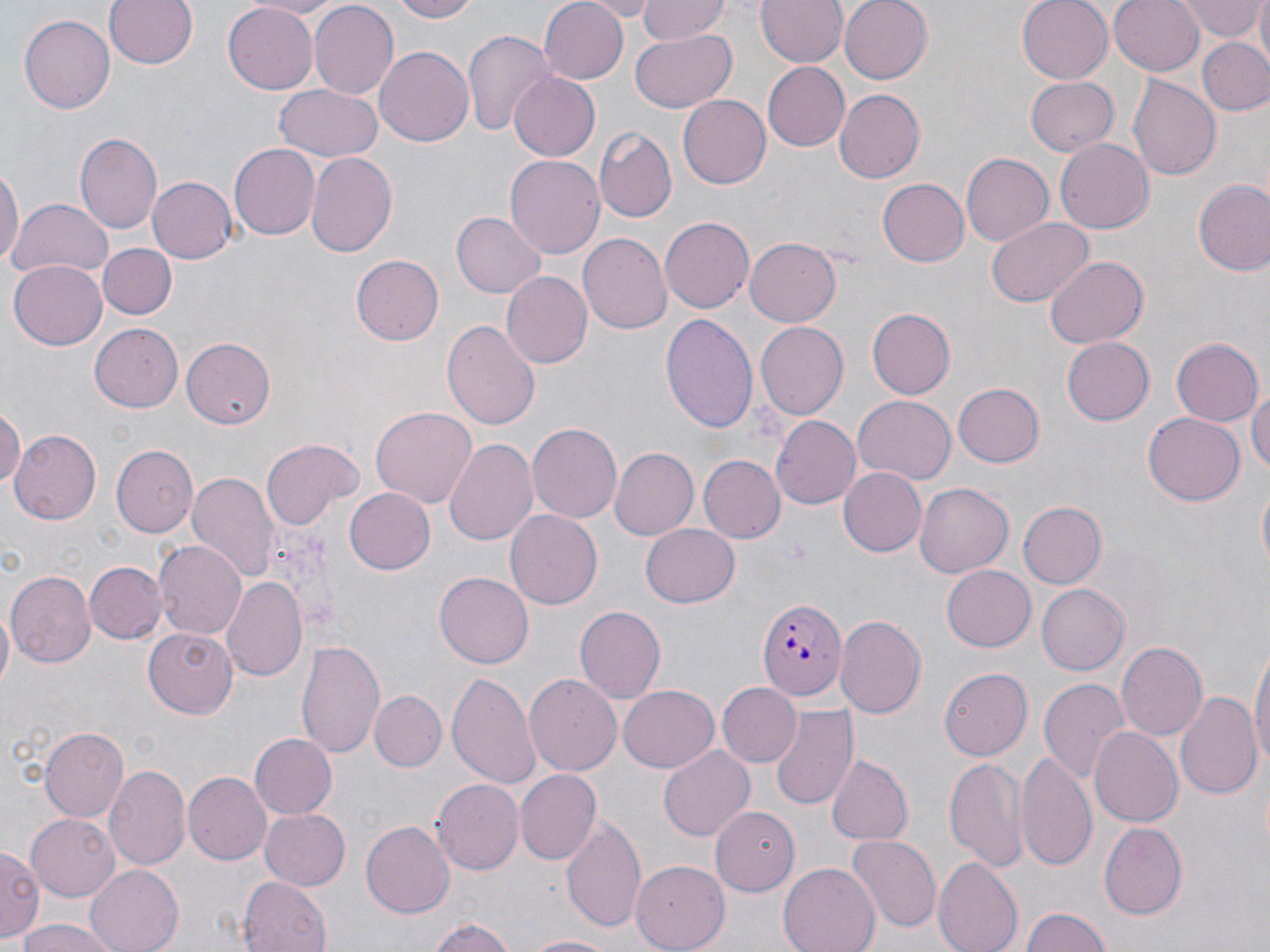

{
  "slide_level_diagnosis": "Plasmodium falciparum",
  "stain": "May-Grünwald-Giemsa",
  "field_of_view": "single",
  "preparation": "thin blood smear",
  "modality": "light microscopy",
  "magnification": "1000x",
  "plasmodium_falciparum_infected_red_blood_cell_locations": "approximate bounding boxes as [x1, y1, x2, y2] in pixels: [755, 598, 847, 703]",
  "uninfected_red_blood_cell_locations": "approximate bounding boxes as [x1, y1, x2, y2] in pixels: [104, 0, 197, 70], [244, 0, 346, 19], [392, 0, 482, 23], [538, 0, 627, 84], [582, 0, 660, 19], [639, 0, 730, 42], [758, 0, 847, 68], [837, 0, 933, 84], [1016, 0, 1113, 84], [1109, 0, 1206, 76], [1253, 0, 1270, 62], [1178, 2, 1266, 41], [309, 3, 398, 98], [220, 4, 319, 93], [19, 15, 116, 113], [461, 29, 556, 138], [630, 30, 736, 112], [1198, 37, 1270, 115], [374, 46, 474, 147], [761, 61, 850, 151], [509, 71, 603, 160], [1128, 74, 1223, 179], [1024, 76, 1119, 155], [273, 84, 380, 162], [834, 89, 925, 183], [677, 92, 770, 186], [595, 127, 675, 221], [75, 133, 162, 237], [1055, 137, 1153, 234], [229, 144, 320, 239], [307, 151, 397, 255], [960, 153, 1054, 246], [505, 156, 604, 258], [0, 160, 22, 277], [146, 176, 238, 264], [879, 178, 969, 267], [1192, 178, 1270, 276], [10, 197, 112, 282], [105, 209, 206, 312], [451, 212, 546, 298], [659, 216, 754, 314], [986, 217, 1092, 307], [579, 234, 672, 336], [744, 237, 842, 327], [96, 242, 176, 320], [351, 255, 443, 344], [1045, 256, 1149, 348], [8, 258, 106, 347], [500, 272, 593, 368], [867, 308, 955, 398], [660, 313, 759, 436], [441, 318, 540, 432], [89, 322, 184, 410], [755, 322, 847, 420], [1060, 336, 1152, 426], [181, 337, 275, 428], [1171, 337, 1264, 427], [952, 383, 1043, 467], [1248, 384, 1270, 476], [852, 397, 955, 483], [0, 405, 24, 492], [370, 407, 475, 510], [771, 413, 861, 508], [1142, 413, 1244, 505], [527, 422, 621, 523], [10, 430, 99, 524], [262, 438, 362, 528], [443, 438, 537, 545], [110, 445, 196, 538], [610, 447, 699, 538], [697, 454, 784, 544], [837, 467, 926, 557], [186, 470, 280, 584], [1255, 477, 1270, 579], [914, 483, 1012, 578], [343, 487, 435, 574], [1016, 500, 1106, 590], [505, 509, 602, 609], [642, 523, 740, 608], [154, 540, 244, 639], [85, 561, 165, 645], [941, 565, 1036, 652], [6, 570, 96, 669], [434, 571, 533, 666], [221, 577, 307, 683], [1036, 583, 1129, 675], [574, 605, 666, 702], [0, 608, 14, 691], [835, 615, 926, 719], [144, 626, 241, 716], [297, 638, 383, 759], [1250, 640, 1270, 773], [1117, 642, 1207, 743], [939, 668, 1033, 761], [447, 671, 539, 790], [525, 674, 621, 777], [1039, 677, 1132, 784], [717, 681, 801, 766], [616, 684, 719, 774], [370, 690, 446, 772], [1175, 691, 1261, 801], [771, 706, 858, 812], [1088, 725, 1183, 828], [40, 727, 130, 823], [248, 734, 337, 820], [658, 745, 754, 840], [1015, 751, 1096, 868], [825, 754, 912, 846], [946, 756, 1028, 870], [105, 765, 190, 873], [516, 770, 600, 865], [184, 772, 271, 866], [429, 778, 523, 872], [710, 806, 799, 897], [261, 807, 349, 887], [26, 813, 121, 899], [560, 814, 647, 931], [360, 821, 454, 918], [1100, 821, 1188, 917], [847, 833, 941, 933], [0, 846, 42, 941], [934, 857, 1021, 952], [630, 859, 730, 951], [779, 861, 881, 952], [86, 864, 184, 952], [238, 876, 333, 952], [1021, 908, 1112, 952], [427, 917, 515, 952], [17, 918, 124, 952], [520, 933, 617, 952]",
  "image_size": "1270×952 pixels"
}